Give the extent of all uninfected red blood cells.
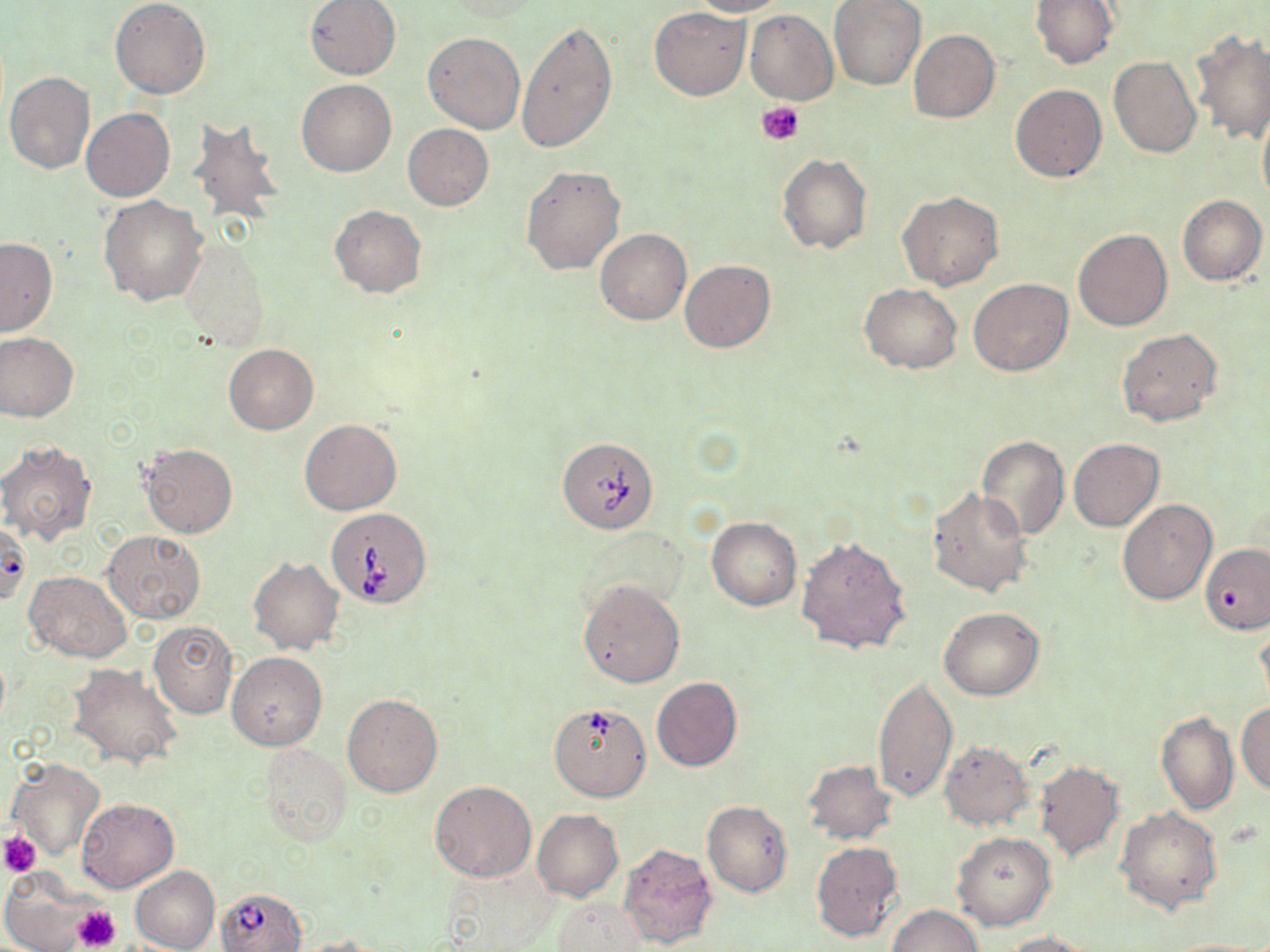
Approximate bounding boxes as named x1/y1/x2/y2 corners in pixels.
Uninfected red blood cells: (x1=110, y1=0, x2=210, y2=99), (x1=305, y1=0, x2=401, y2=80), (x1=690, y1=0, x2=786, y2=16), (x1=829, y1=0, x2=925, y2=90), (x1=1030, y1=0, x2=1119, y2=69), (x1=650, y1=7, x2=749, y2=100), (x1=745, y1=10, x2=839, y2=105), (x1=516, y1=20, x2=617, y2=154), (x1=910, y1=30, x2=1000, y2=122), (x1=1192, y1=30, x2=1270, y2=145), (x1=423, y1=31, x2=526, y2=133), (x1=1109, y1=57, x2=1201, y2=158), (x1=4, y1=72, x2=97, y2=174), (x1=296, y1=80, x2=396, y2=177), (x1=1011, y1=84, x2=1107, y2=182), (x1=1257, y1=105, x2=1270, y2=208), (x1=82, y1=108, x2=175, y2=202), (x1=187, y1=115, x2=285, y2=229), (x1=402, y1=123, x2=494, y2=210), (x1=778, y1=154, x2=871, y2=253), (x1=519, y1=165, x2=625, y2=276), (x1=897, y1=191, x2=1003, y2=290), (x1=1178, y1=195, x2=1267, y2=285), (x1=99, y1=196, x2=208, y2=305), (x1=329, y1=205, x2=426, y2=297), (x1=595, y1=228, x2=691, y2=325), (x1=1074, y1=229, x2=1172, y2=331), (x1=0, y1=237, x2=58, y2=337), (x1=178, y1=239, x2=268, y2=351), (x1=679, y1=259, x2=775, y2=353), (x1=969, y1=278, x2=1072, y2=377), (x1=860, y1=283, x2=962, y2=373), (x1=1117, y1=329, x2=1222, y2=427), (x1=0, y1=332, x2=79, y2=422), (x1=224, y1=344, x2=319, y2=435), (x1=300, y1=419, x2=402, y2=515), (x1=976, y1=435, x2=1069, y2=540), (x1=1068, y1=438, x2=1163, y2=532), (x1=0, y1=441, x2=97, y2=544), (x1=142, y1=443, x2=238, y2=537), (x1=927, y1=487, x2=1033, y2=598), (x1=1116, y1=498, x2=1217, y2=604), (x1=707, y1=516, x2=801, y2=611), (x1=102, y1=530, x2=205, y2=622), (x1=796, y1=534, x2=911, y2=656), (x1=1201, y1=544, x2=1270, y2=634), (x1=249, y1=558, x2=344, y2=655), (x1=26, y1=571, x2=131, y2=662), (x1=577, y1=579, x2=685, y2=688), (x1=940, y1=608, x2=1043, y2=699), (x1=1255, y1=619, x2=1270, y2=712), (x1=148, y1=621, x2=239, y2=718), (x1=228, y1=652, x2=329, y2=752), (x1=67, y1=664, x2=183, y2=770), (x1=872, y1=675, x2=958, y2=803), (x1=652, y1=678, x2=743, y2=771), (x1=342, y1=693, x2=442, y2=796), (x1=1235, y1=700, x2=1270, y2=796), (x1=1155, y1=712, x2=1238, y2=816), (x1=939, y1=740, x2=1032, y2=832), (x1=258, y1=743, x2=352, y2=844), (x1=7, y1=758, x2=106, y2=863), (x1=802, y1=759, x2=896, y2=844), (x1=1034, y1=759, x2=1125, y2=862), (x1=430, y1=780, x2=538, y2=882), (x1=76, y1=797, x2=179, y2=892), (x1=702, y1=802, x2=794, y2=897), (x1=1116, y1=807, x2=1222, y2=914), (x1=533, y1=809, x2=623, y2=901), (x1=952, y1=831, x2=1056, y2=931), (x1=811, y1=841, x2=903, y2=943), (x1=618, y1=842, x2=718, y2=950), (x1=439, y1=865, x2=558, y2=950), (x1=1, y1=866, x2=100, y2=952), (x1=132, y1=866, x2=220, y2=952), (x1=553, y1=898, x2=649, y2=951), (x1=886, y1=904, x2=982, y2=952), (x1=999, y1=930, x2=1091, y2=951), (x1=288, y1=935, x2=389, y2=951), (x1=1163, y1=938, x2=1267, y2=951).

Platelet locations: (x1=758, y1=101, x2=805, y2=145), (x1=0, y1=831, x2=41, y2=876), (x1=72, y1=904, x2=122, y2=950). Babesia divergens-infected red blood cell locations: (x1=557, y1=436, x2=658, y2=534), (x1=319, y1=506, x2=433, y2=608), (x1=553, y1=704, x2=651, y2=804), (x1=215, y1=888, x2=309, y2=952). Slide-level diagnosis: Babesia divergens. One field of a larger specimen. May-Grünwald-Giemsa stain. 1000x magnification. Light microscopy. Thin blood smear. Image is 1270×952 pixels.